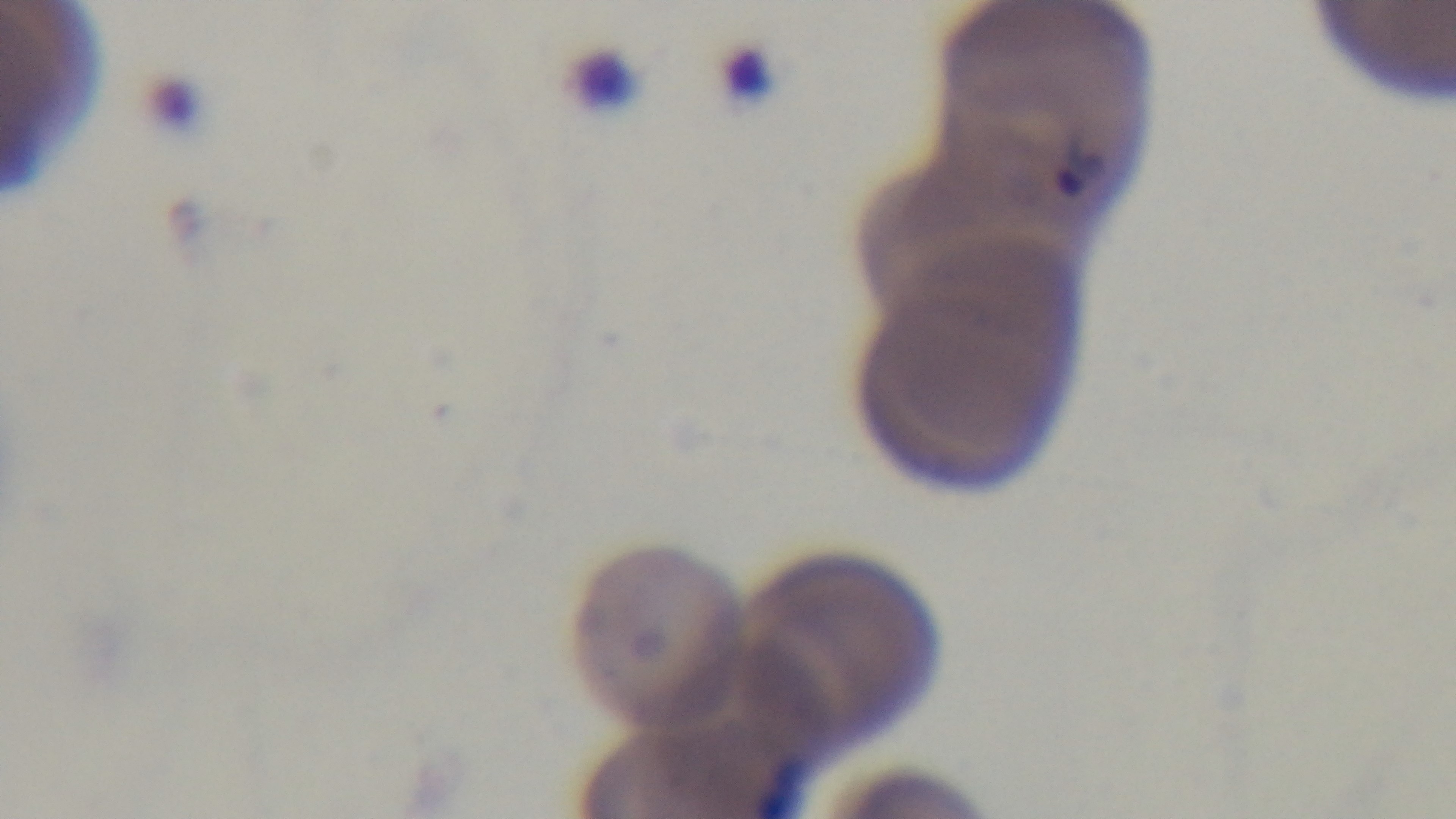

Captured with a mounted 4K digital camera. Giemsa-stained. Oil-immersion objective, 100x. One field from the slide. Malaria status: positive. Preparation: thin blood film. Photomicrograph.